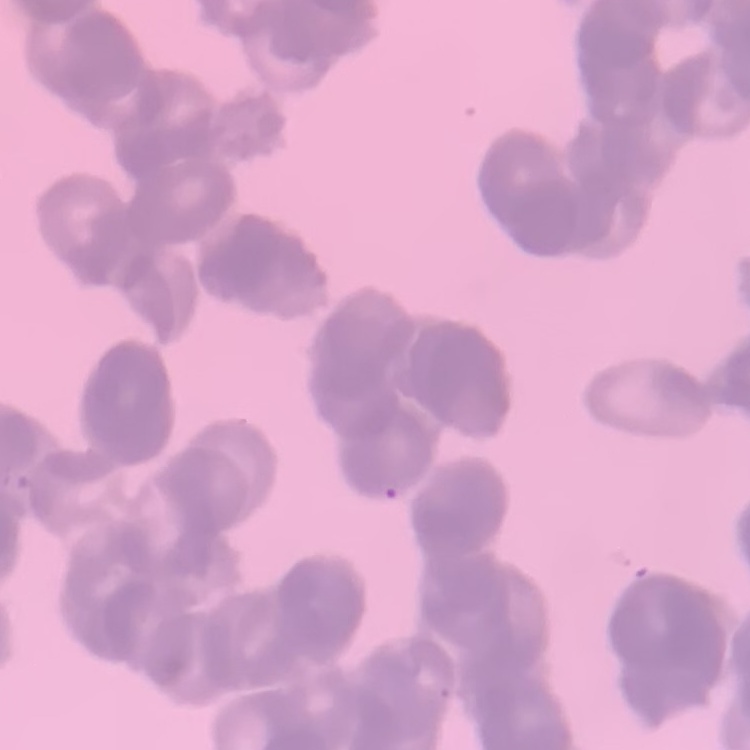
The red blood cells exhibit rouleaux formation. Field's or Giemsa stain. One tile cut from a larger photomicrograph. Thin blood film.